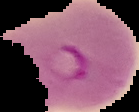

Summary:
  - Image type: cell region segmented out of the field of view; surrounding area masked to black
  - Preparation: thin blood film
  - Malaria status: parasitized
  - Image size: 139×112 pixels